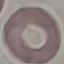

result: no malaria parasites seen
stain: Giemsa
preparation: thin blood smear
image_type: automatically extracted cell patch, resized to 64 × 64 pixels
capture: smartphone camera at the microscope eyepiece